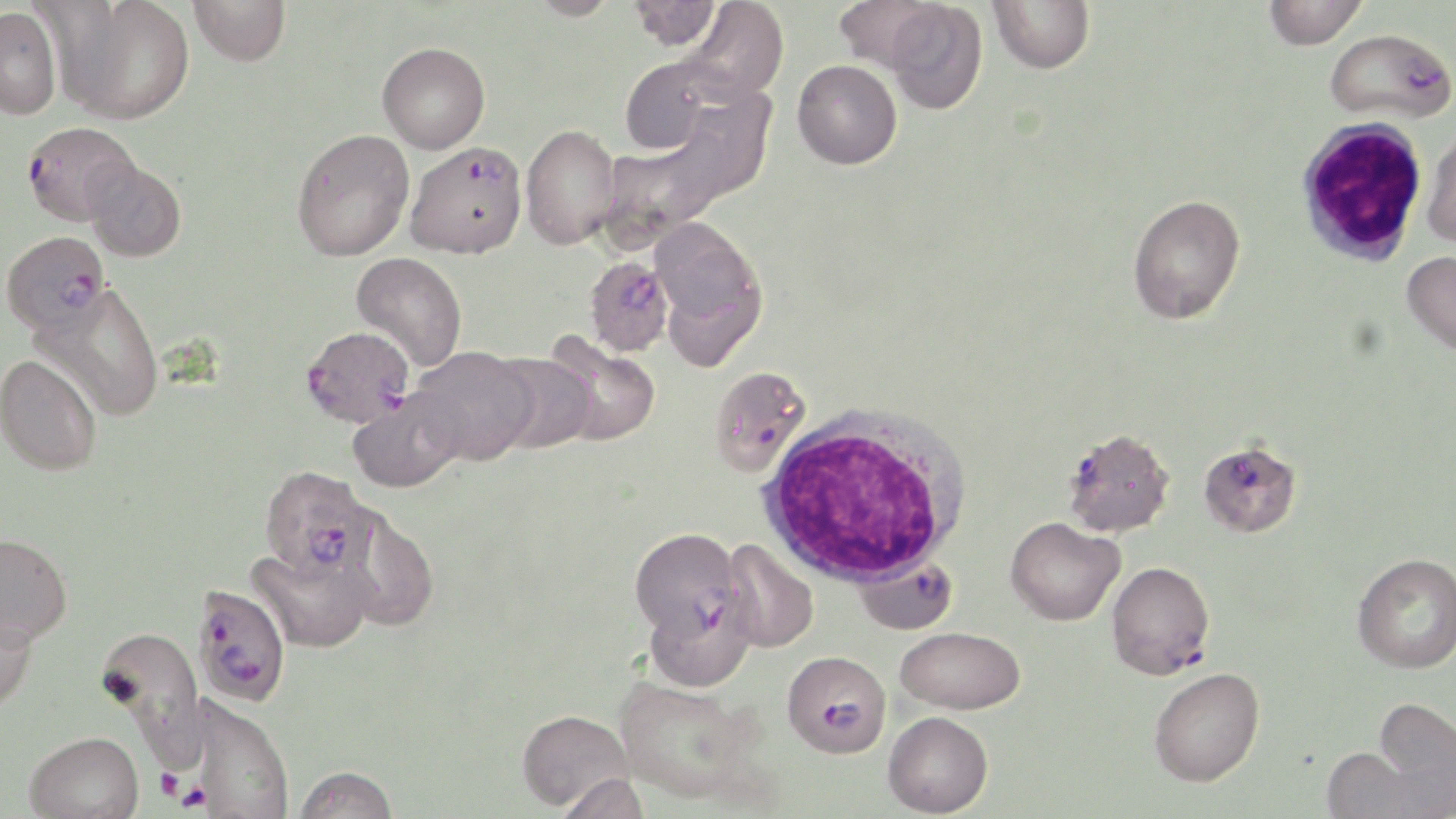 Approximate bounding boxes as named x1/y1/x2/y2 corners in pixels. Uninfected red blood cell locations: (x1=60, y1=0, x2=195, y2=125), (x1=189, y1=0, x2=290, y2=66), (x1=524, y1=0, x2=622, y2=21), (x1=627, y1=0, x2=723, y2=51), (x1=682, y1=0, x2=789, y2=102), (x1=831, y1=0, x2=949, y2=75), (x1=883, y1=0, x2=988, y2=114), (x1=988, y1=0, x2=1095, y2=74), (x1=1264, y1=0, x2=1367, y2=50), (x1=0, y1=6, x2=63, y2=120), (x1=377, y1=42, x2=490, y2=153), (x1=618, y1=55, x2=722, y2=155), (x1=792, y1=59, x2=902, y2=169), (x1=520, y1=123, x2=622, y2=250), (x1=1422, y1=124, x2=1456, y2=248), (x1=291, y1=130, x2=415, y2=262), (x1=83, y1=158, x2=187, y2=262), (x1=1127, y1=194, x2=1245, y2=324), (x1=650, y1=218, x2=764, y2=339), (x1=1402, y1=250, x2=1456, y2=356), (x1=351, y1=252, x2=468, y2=371), (x1=32, y1=284, x2=165, y2=422), (x1=543, y1=334, x2=661, y2=446), (x1=411, y1=346, x2=538, y2=464), (x1=489, y1=352, x2=596, y2=453), (x1=0, y1=354, x2=102, y2=476), (x1=346, y1=389, x2=466, y2=493), (x1=338, y1=508, x2=439, y2=633), (x1=1005, y1=516, x2=1124, y2=626), (x1=0, y1=532, x2=72, y2=646), (x1=720, y1=539, x2=820, y2=653), (x1=248, y1=545, x2=376, y2=653), (x1=1352, y1=552, x2=1456, y2=674), (x1=644, y1=590, x2=756, y2=692), (x1=0, y1=609, x2=38, y2=714), (x1=95, y1=626, x2=208, y2=764), (x1=895, y1=626, x2=1025, y2=715), (x1=1149, y1=667, x2=1264, y2=786), (x1=614, y1=676, x2=758, y2=801), (x1=182, y1=695, x2=295, y2=819), (x1=1373, y1=696, x2=1456, y2=810), (x1=516, y1=709, x2=633, y2=811), (x1=883, y1=711, x2=993, y2=817), (x1=24, y1=730, x2=144, y2=819), (x1=1321, y1=745, x2=1427, y2=819), (x1=293, y1=765, x2=399, y2=819), (x1=557, y1=772, x2=651, y2=819). Plasmodium falciparum-infected red blood cell locations: (x1=1325, y1=29, x2=1455, y2=123), (x1=22, y1=121, x2=139, y2=226), (x1=405, y1=141, x2=527, y2=258), (x1=2, y1=230, x2=110, y2=334), (x1=584, y1=257, x2=674, y2=356), (x1=301, y1=325, x2=415, y2=428), (x1=708, y1=364, x2=812, y2=478), (x1=1062, y1=427, x2=1175, y2=538), (x1=1203, y1=452, x2=1300, y2=541), (x1=258, y1=465, x2=377, y2=583), (x1=629, y1=527, x2=742, y2=641), (x1=851, y1=554, x2=959, y2=634), (x1=1106, y1=561, x2=1215, y2=679), (x1=189, y1=584, x2=291, y2=707), (x1=782, y1=650, x2=890, y2=757). Platelet locations: (x1=156, y1=768, x2=185, y2=803), (x1=174, y1=778, x2=213, y2=814). White blood cell locations: (x1=1294, y1=115, x2=1430, y2=267), (x1=757, y1=407, x2=968, y2=588). Slide-level diagnosis: Plasmodium falciparum. Image is 1456×819 pixels. Single field of view. May-Grünwald-Giemsa stain. Thin blood film. 1000x magnification. Optical microscopy.